Locate every blood parasite and identify its species.
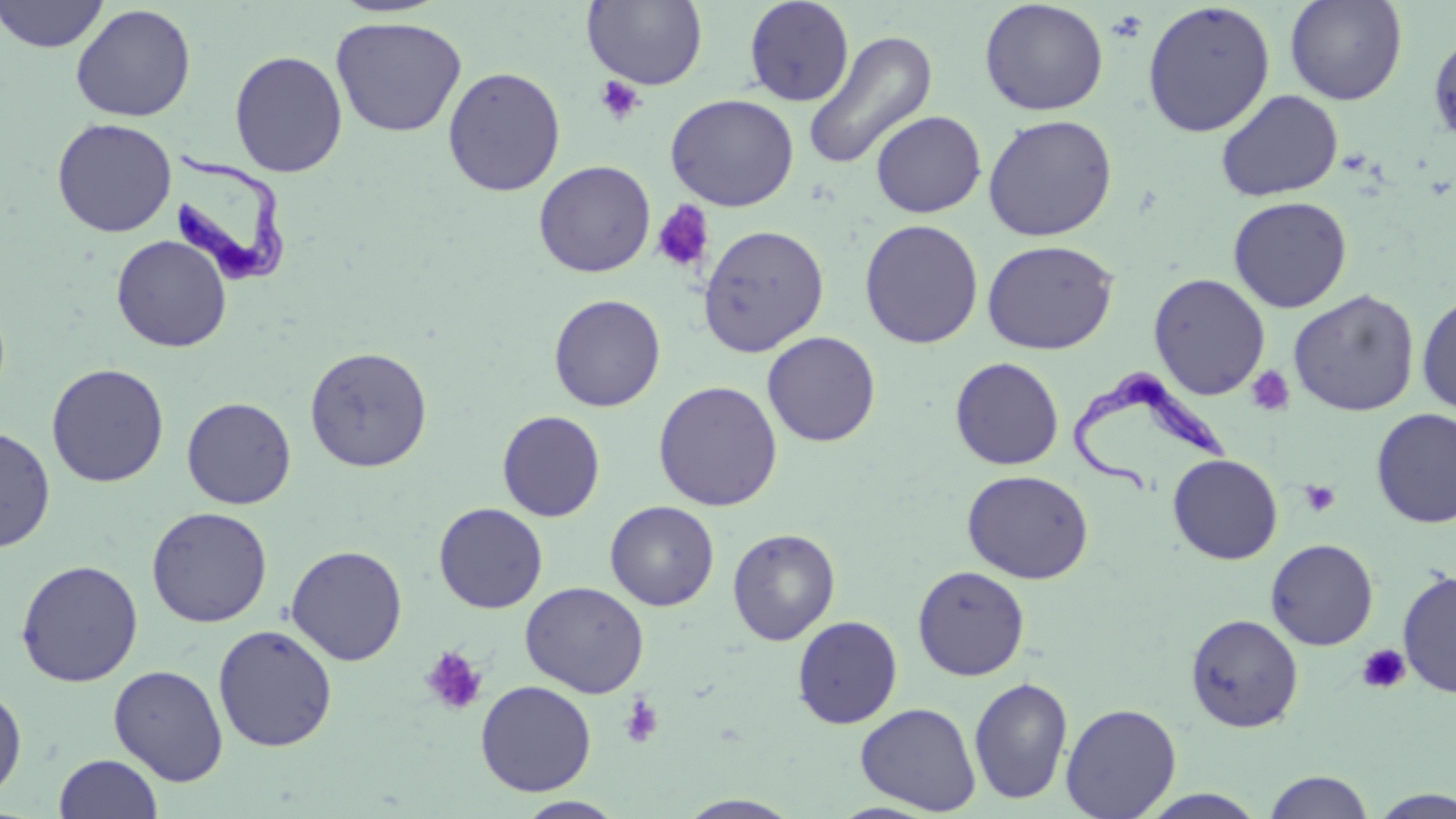

Approximate bounding boxes as [x1, y1, x2, y2] in pixels.
Trypanosoma brucei: [164, 155, 293, 290], [1070, 367, 1241, 495].
No Plasmodium falciparum, Plasmodium ovale, Plasmodium malariae, Plasmodium vivax, or Babesia divergens observed.

Summary:
  - Uninfected red blood cell locations: [0, 0, 109, 53], [582, 0, 708, 89], [744, 0, 854, 107], [1285, 0, 1408, 105], [979, 1, 1109, 116], [1141, 2, 1276, 137], [71, 4, 196, 122], [330, 16, 468, 137], [802, 29, 938, 171], [1428, 29, 1456, 147], [229, 50, 348, 177], [443, 66, 566, 196], [1215, 89, 1343, 201], [665, 93, 799, 211], [870, 110, 986, 218], [982, 114, 1118, 241], [51, 117, 177, 237], [534, 160, 656, 278], [1228, 195, 1352, 313], [859, 219, 984, 348], [697, 223, 830, 357], [111, 234, 232, 353], [982, 239, 1119, 355], [1148, 273, 1270, 400], [1288, 289, 1419, 417], [1416, 290, 1456, 416], [548, 294, 666, 412], [762, 331, 881, 447], [304, 345, 433, 472], [950, 356, 1064, 470], [46, 363, 169, 488], [653, 380, 782, 511], [181, 396, 296, 509], [1371, 407, 1456, 529], [497, 410, 606, 522], [0, 425, 56, 553], [1167, 454, 1283, 565], [962, 469, 1094, 584], [605, 500, 719, 611], [433, 502, 548, 613], [146, 506, 272, 627], [727, 528, 840, 646], [1265, 538, 1379, 650], [286, 544, 408, 666], [15, 559, 143, 687], [912, 565, 1030, 681], [1397, 569, 1456, 698], [520, 581, 649, 698], [1185, 613, 1304, 732], [792, 615, 903, 728], [213, 624, 338, 752], [108, 664, 228, 786], [969, 676, 1073, 805], [475, 680, 597, 796], [0, 683, 27, 801], [855, 702, 981, 814], [1061, 703, 1182, 818], [54, 753, 162, 818], [1263, 770, 1375, 818], [1137, 789, 1269, 818], [1369, 789, 1456, 818], [675, 794, 805, 818], [514, 796, 627, 818], [826, 802, 944, 819]
  - Platelet locations: [594, 75, 645, 126], [651, 201, 715, 273], [1245, 366, 1295, 416], [1299, 479, 1342, 517], [1356, 644, 1411, 694], [420, 646, 489, 716], [619, 694, 664, 749]
  - Slide-level diagnosis: Trypanosoma brucei
  - Image size: 1456×819 pixels
  - Preparation: thin blood smear
  - Stain: May-Grünwald-Giemsa
  - Magnification: 1000x
  - Field of view: single
  - Modality: light microscopy